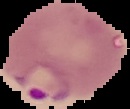
From a thin blood film. Cell region segmented out of the field of view; the surrounding area is masked to black. Malaria status: parasitized. Image is 130×109 pixels.